Locate every Plasmodium parasite.
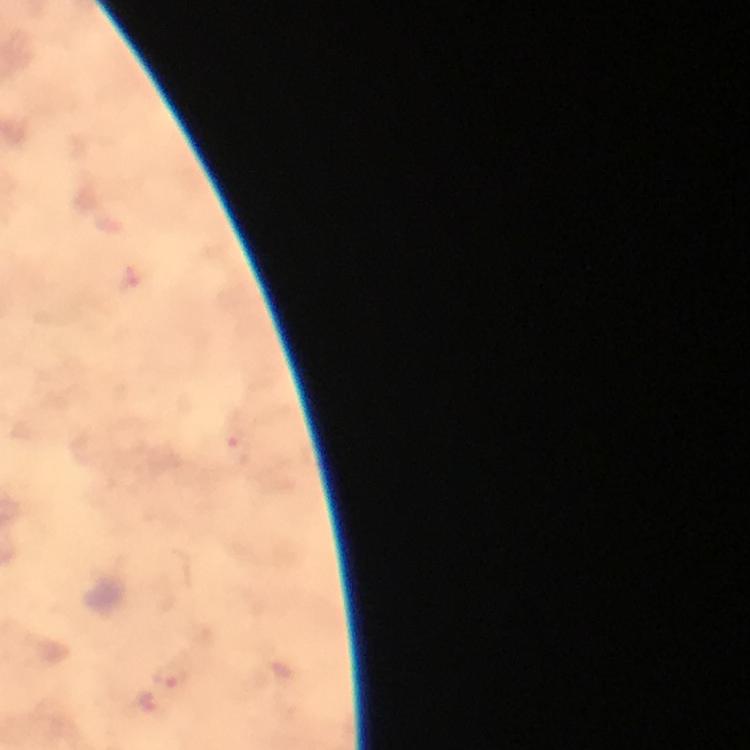

Approximate centers as {x, y} in pixels.
Plasmodium parasites: {171, 676}.

Summary:
  - Context: from a diagnostic examination for malaria
  - Stain: Giemsa
  - Cropped from: a single field of view
  - Immersion oil: applied
  - Magnification: 100x
  - Capture: smartphone mounted on the microscope
  - Image size: 750×750 pixels
  - Preparation: thick smear